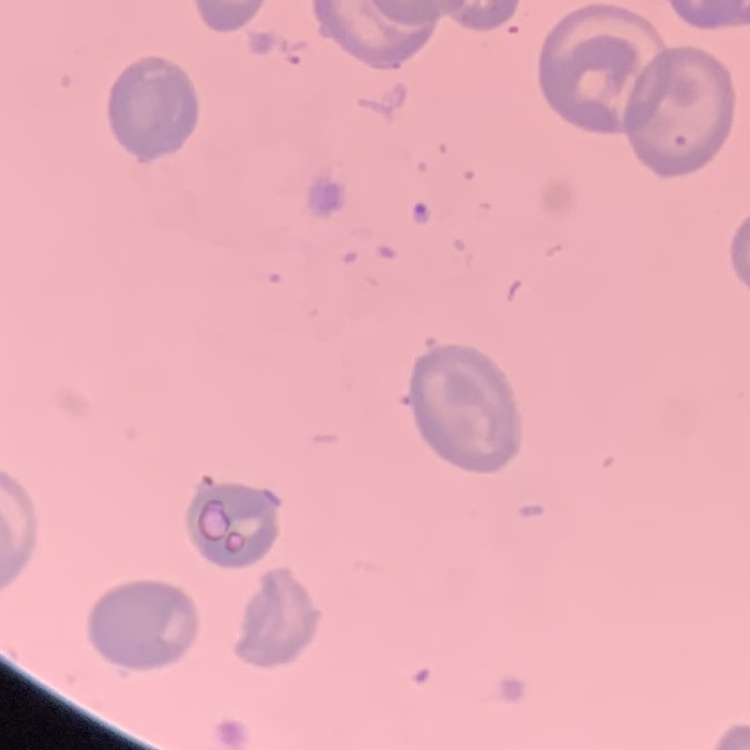
Summary:
  - Red blood cell morphology: no rouleaux formation
  - Preparation: thin blood film
  - Stain: Field's or Giemsa
  - Image type: one tile cut from a larger photomicrograph